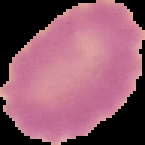

{
  "image_size": "145×145 pixels",
  "image_type": "segmented cell region on a black background",
  "result": "no Plasmodium parasites seen",
  "preparation": "thin blood film"
}